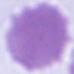

An erythrocyte is seen. 1000x magnification. Micrograph.